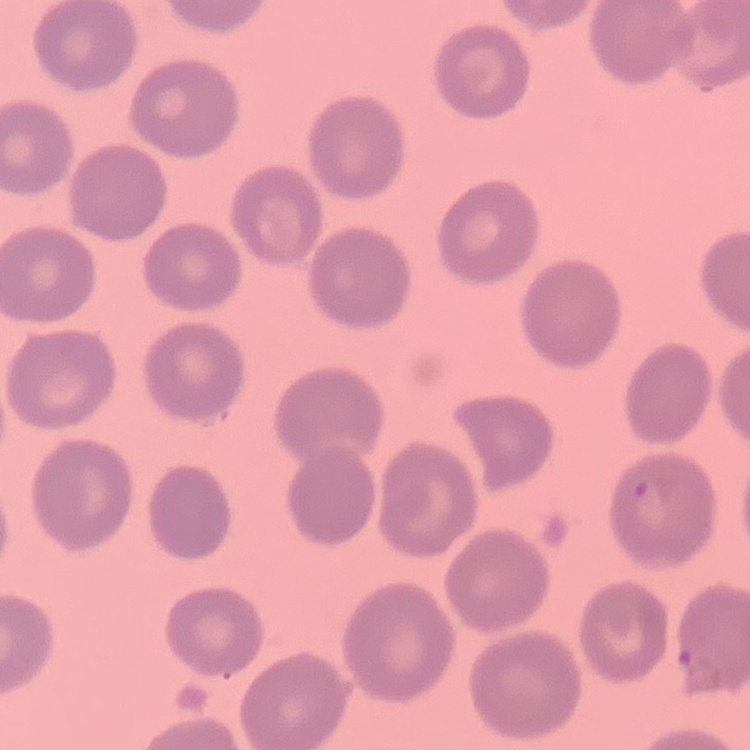
erythrocyte morphology = no rouleaux formation
preparation = thin blood film
image type = square crop of a larger photomicrograph
stain = Field's or Giemsa